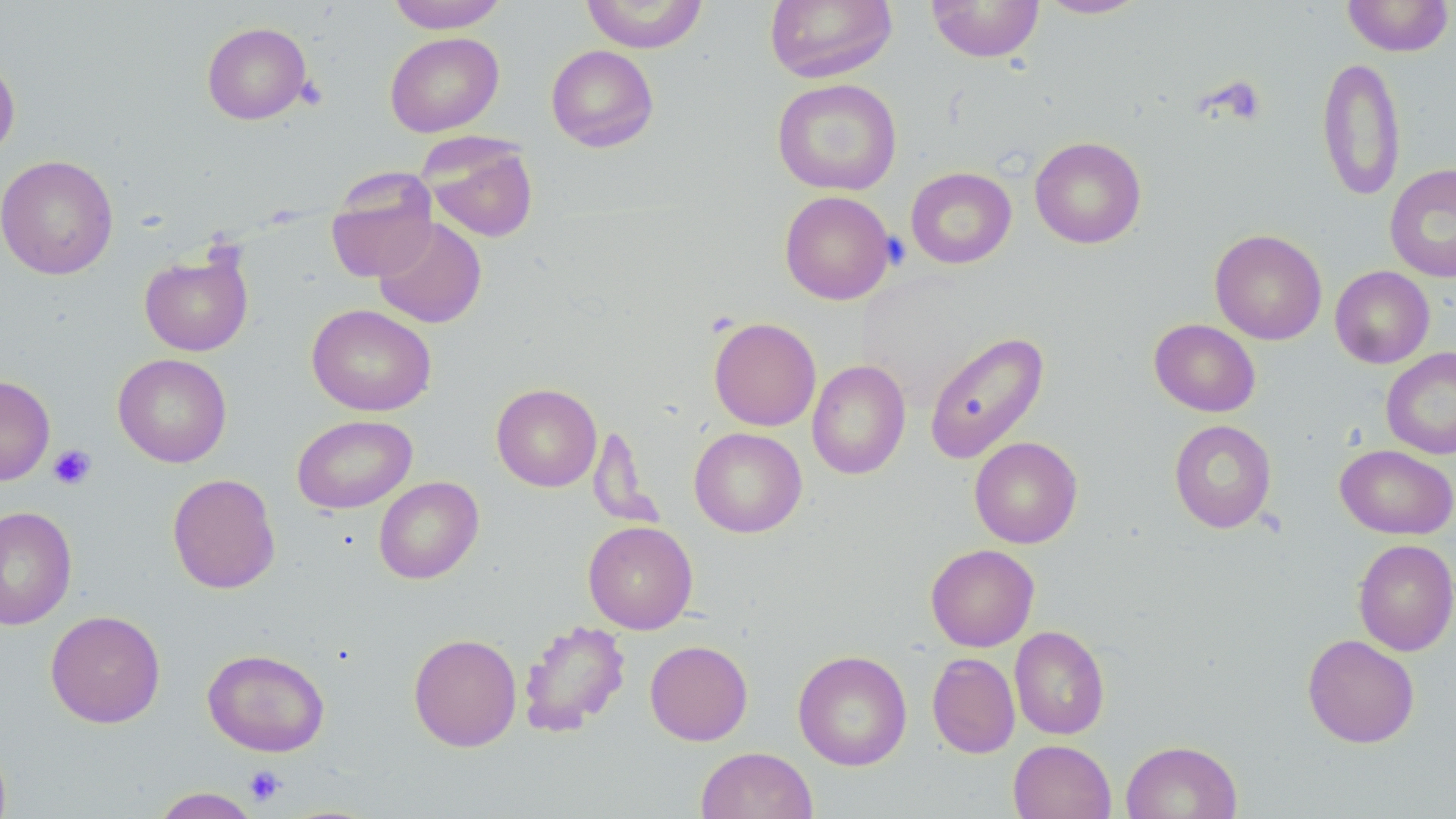
slide-level diagnosis = negative for blood parasites
modality = light microscopy
stain = May-Grünwald-Giemsa
platelet locations = approximate bounding boxes as (x1, y1, x2, y2) in pixels: (295, 76, 328, 110), (881, 233, 911, 271), (48, 444, 97, 490), (244, 766, 285, 806)
uninfected red blood cell locations = approximate bounding boxes as (x1, y1, x2, y2) in pixels: (386, 0, 509, 33), (580, 0, 709, 53), (764, 0, 898, 84), (1037, 0, 1150, 19), (1342, 0, 1454, 57), (926, 1, 1045, 62), (201, 22, 312, 125), (385, 32, 504, 137), (546, 44, 659, 152), (0, 55, 20, 160), (1317, 55, 1405, 201), (772, 78, 902, 195), (421, 135, 539, 243), (1029, 136, 1147, 249), (1, 155, 119, 280), (1385, 163, 1456, 282), (905, 167, 1016, 269), (326, 175, 438, 283), (779, 190, 896, 305), (373, 217, 487, 328), (1210, 229, 1327, 345), (139, 245, 254, 357), (1330, 266, 1435, 368), (307, 303, 436, 416), (708, 317, 821, 431), (1149, 318, 1261, 417), (924, 331, 1050, 464), (1380, 347, 1456, 460), (113, 353, 232, 467), (807, 359, 911, 480), (0, 374, 55, 486), (491, 383, 602, 492), (292, 415, 417, 514), (1169, 419, 1277, 533), (588, 426, 660, 529), (689, 427, 807, 537), (969, 436, 1083, 549), (1335, 444, 1456, 539), (167, 473, 281, 594), (374, 476, 484, 583), (0, 506, 76, 630), (583, 520, 698, 634), (1353, 539, 1456, 655), (925, 544, 1039, 652), (45, 610, 165, 728), (518, 619, 631, 737), (1009, 625, 1110, 739), (408, 632, 522, 752), (1302, 633, 1420, 748), (645, 640, 753, 745), (202, 648, 330, 757), (792, 650, 912, 770), (927, 652, 1020, 758), (1008, 740, 1116, 819), (1121, 740, 1242, 819), (695, 746, 817, 819), (150, 787, 261, 818)
magnification = 1000x
image size = 1456×819 pixels
preparation = thin blood film
field of view = single